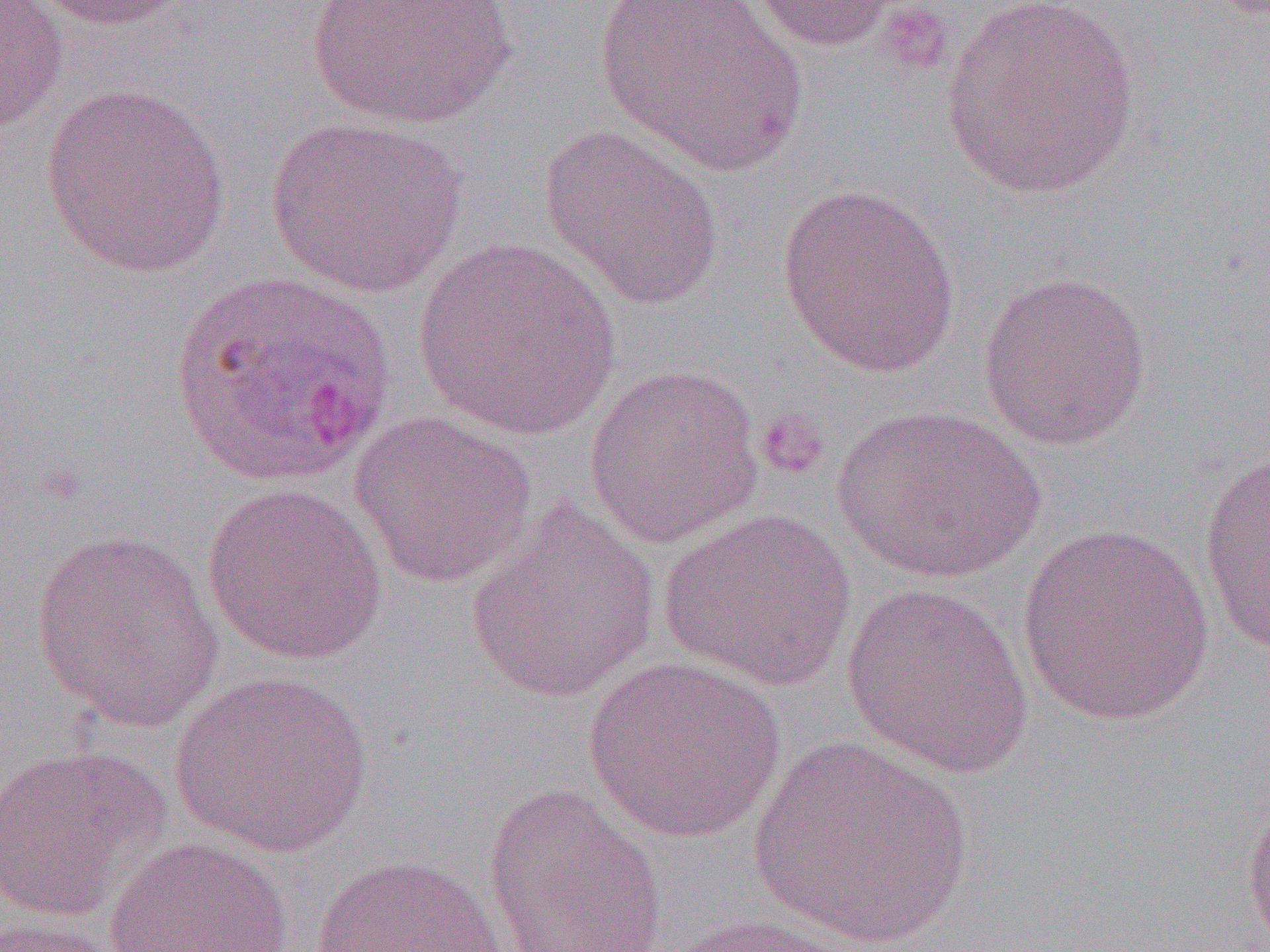
Summary:
  - Coordinate format: approximate bounding boxes as named x1/y1/x2/y2 corners in pixels
  - Plasmodium ovale-infected red blood cell locations: (x1=171, y1=269, x2=396, y2=488)
  - Uninfected red blood cell locations: (x1=0, y1=0, x2=69, y2=138), (x1=28, y1=0, x2=198, y2=31), (x1=307, y1=0, x2=517, y2=129), (x1=595, y1=0, x2=809, y2=178), (x1=742, y1=0, x2=914, y2=51), (x1=940, y1=1, x2=1142, y2=200), (x1=40, y1=84, x2=231, y2=277), (x1=266, y1=115, x2=466, y2=298), (x1=538, y1=123, x2=725, y2=309), (x1=776, y1=182, x2=962, y2=377), (x1=413, y1=238, x2=623, y2=441), (x1=977, y1=271, x2=1152, y2=450), (x1=584, y1=363, x2=764, y2=548), (x1=833, y1=403, x2=1046, y2=584), (x1=348, y1=411, x2=538, y2=588), (x1=1198, y1=448, x2=1270, y2=657), (x1=202, y1=483, x2=388, y2=666), (x1=466, y1=501, x2=659, y2=704), (x1=658, y1=507, x2=856, y2=692), (x1=1017, y1=524, x2=1217, y2=726), (x1=29, y1=526, x2=225, y2=735), (x1=841, y1=583, x2=1034, y2=779), (x1=581, y1=656, x2=788, y2=843), (x1=169, y1=669, x2=374, y2=859), (x1=751, y1=734, x2=973, y2=950), (x1=0, y1=745, x2=169, y2=921), (x1=483, y1=782, x2=668, y2=952), (x1=1240, y1=787, x2=1270, y2=950), (x1=104, y1=837, x2=294, y2=952), (x1=310, y1=853, x2=513, y2=952), (x1=658, y1=912, x2=875, y2=952), (x1=0, y1=917, x2=136, y2=952)
  - Platelet locations: (x1=875, y1=2, x2=957, y2=76), (x1=755, y1=409, x2=830, y2=481)
  - Slide-level diagnosis: Plasmodium ovale
  - Image size: 1270×952 pixels
  - Preparation: thin blood smear
  - Modality: light microscopy
  - Field of view: single
  - Magnification: 1000x